State the preparation type.
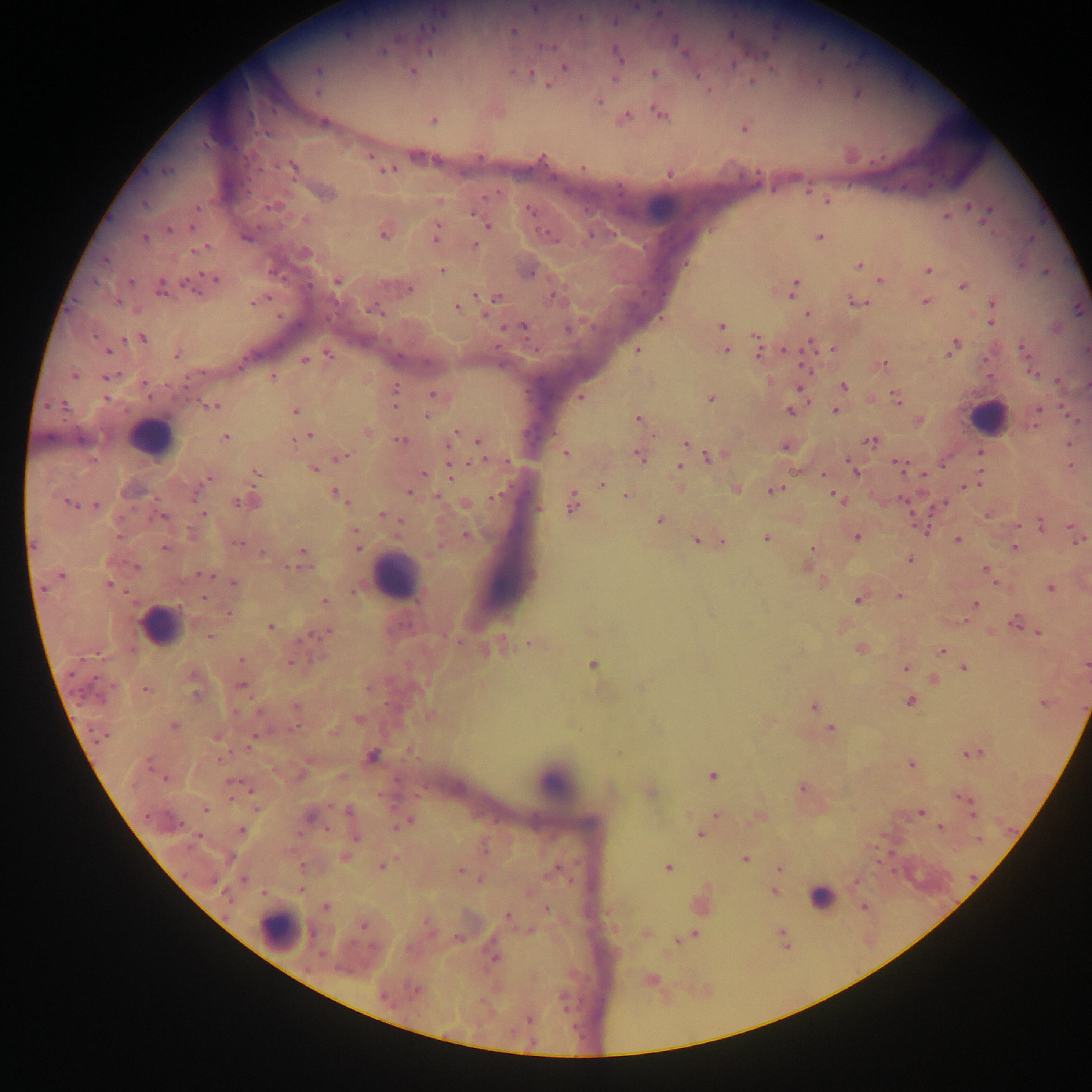
Thick blood smear.

Approximate centers as {x, y} in pixels.
Summary:
  - Plasmodium parasite locations: {534, 8}, {580, 17}, {514, 30}, {679, 45}, {383, 50}, {618, 55}, {733, 64}, {564, 66}, {317, 70}, {412, 72}, {654, 72}, {529, 73}, {615, 76}, {752, 81}, {547, 84}, {857, 93}, {599, 101}, {660, 112}, {624, 117}, {431, 120}, {323, 123}, {745, 126}, {292, 167}, {583, 167}, {387, 169}, {166, 170}, {669, 173}, {324, 193}, {438, 200}, {827, 201}, {970, 206}, {271, 207}, {530, 210}, {945, 215}, {986, 217}, {482, 221}, {488, 225}, {192, 226}, {168, 230}, {383, 232}, {437, 235}, {819, 237}, {144, 238}, {474, 244}, {199, 249}, {859, 266}, {441, 270}, {928, 270}, {1046, 271}, {212, 278}, {880, 279}, {129, 281}, {336, 281}, {190, 285}, {962, 285}, {161, 287}, {408, 288}, {792, 288}, {553, 295}, {496, 297}, {255, 300}, {855, 301}, {925, 301}, {993, 301}, {118, 302}, {457, 307}, {373, 309}, {1078, 309}, {808, 313}, {486, 314}, {992, 322}, {523, 326}, {720, 326}, {141, 338}, {811, 344}, {953, 346}, {759, 347}, {832, 348}, {1022, 348}, {636, 349}, {108, 350}, {725, 350}, {784, 350}, {1086, 350}, {176, 355}, {328, 355}, {304, 359}, {882, 365}, {1034, 373}, {74, 375}, {273, 375}, {109, 376}, {1057, 380}, {1087, 385}, {843, 386}, {800, 388}, {395, 391}, {431, 394}, {580, 396}, {710, 398}, {896, 398}, {394, 402}, {213, 406}, {1062, 407}, {790, 410}, {836, 410}, {1038, 410}, {294, 411}, {426, 415}, {637, 419}, {918, 420}, {1076, 420}, {366, 432}, {455, 432}, {225, 436}, {307, 436}, {297, 439}, {400, 439}, {478, 440}, {871, 440}, {686, 443}, {1068, 444}, {785, 446}, {979, 452}, {566, 453}, {640, 455}, {341, 456}, {710, 456}, {448, 458}, {942, 463}, {900, 465}, {1071, 465}, {679, 467}, {451, 468}, {314, 469}, {855, 471}, {256, 473}, {423, 473}, {822, 474}, {207, 479}, {977, 481}, {602, 483}, {968, 486}, {734, 488}, {773, 489}, {410, 493}, {338, 495}, {626, 495}, {436, 496}, {837, 496}, {495, 497}, {247, 501}, {571, 501}, {943, 503}, {70, 504}, {465, 504}, {95, 505}, {538, 508}, {203, 513}, {382, 514}, {986, 514}, {162, 516}, {659, 520}, {1041, 524}, {1017, 525}, {926, 529}, {1074, 529}, {355, 532}, {466, 535}, {856, 535}, {766, 537}, {1077, 537}, {957, 539}, {696, 540}, {721, 541}, {237, 544}, {356, 544}, {1014, 547}, {163, 548}, {812, 548}, {261, 552}, {301, 556}, {910, 559}, {807, 565}, {135, 567}, {986, 569}, {60, 575}, {204, 575}, {233, 582}, {823, 583}, {995, 583}, {109, 585}, {1050, 588}, {353, 590}, {898, 595}, {202, 596}, {858, 598}, {324, 601}, {975, 603}, {228, 613}, {965, 621}, {1016, 621}, {270, 626}, {327, 632}, {1038, 632}, {990, 633}, {209, 636}, {530, 643}, {859, 648}, {490, 650}, {942, 650}, {240, 660}, {593, 664}, {1085, 664}, {905, 668}, {964, 668}, {934, 680}, {240, 686}, {368, 686}, {641, 686}, {145, 690}, {910, 700}, {1044, 703}, {814, 705}, {295, 708}, {359, 719}, {173, 726}, {829, 727}, {216, 736}, {254, 737}, {971, 753}, {371, 755}, {910, 763}, {713, 775}, {339, 776}, {164, 779}, {232, 783}, {801, 787}, {649, 791}, {962, 797}, {205, 808}, {971, 810}, {350, 812}, {920, 812}, {715, 814}, {310, 815}, {757, 817}, {404, 822}, {940, 827}, {240, 830}, {700, 834}, {354, 836}, {484, 848}, {344, 857}, {744, 858}, {877, 861}, {302, 866}, {382, 866}, {667, 867}, {779, 868}, {459, 870}, {480, 879}, {855, 880}, {301, 889}, {773, 891}, {863, 906}, {326, 907}, {546, 909}, {508, 917}, {363, 925}, {645, 932}, {782, 933}, {694, 934}, {458, 938}, {784, 939}, {677, 940}, {649, 979}, {415, 990}, {528, 1019}
  - Leukocyte locations: {661, 209}, {988, 417}, {150, 438}, {394, 576}, {160, 625}, {554, 783}, {927, 878}, {821, 897}, {279, 930}
  - Image size: 1092×1092 pixels
  - Field of view: single
  - Capture: mobile-phone photograph through a microscope
  - Country: Ghana